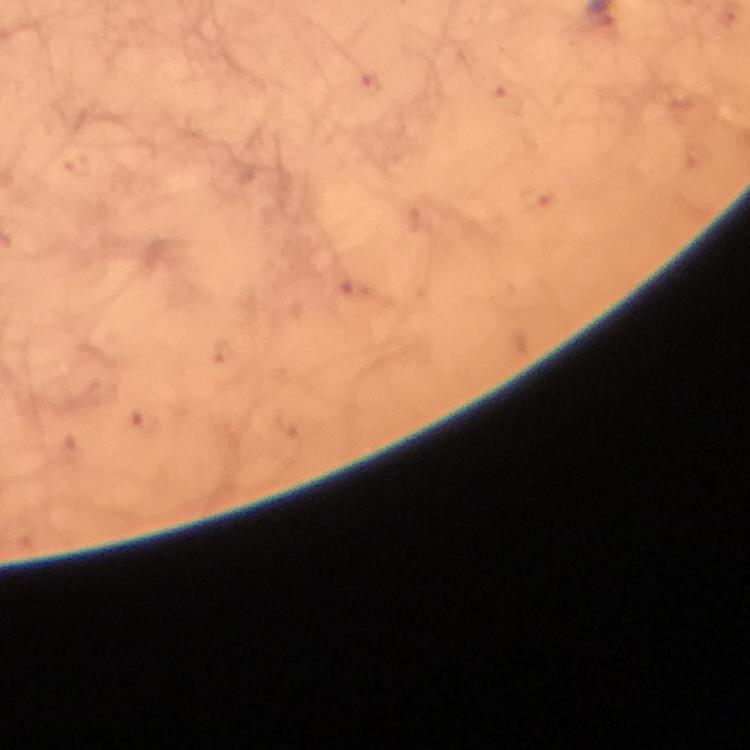

image size = 750×750 pixels
preparation = thick smear
cropped from = one field of view
immersion oil = used
malaria parasite locations = approximate centers as {x, y} in pixels: {370, 83}, {508, 102}, {77, 164}, {536, 199}, {357, 293}, {220, 349}, {143, 422}
magnification = 100x
stain = Giemsa
capture = smartphone photograph through a microscope
context = from a diagnostic examination for malaria